Locate every Plasmodium parasite and every leukocyte.
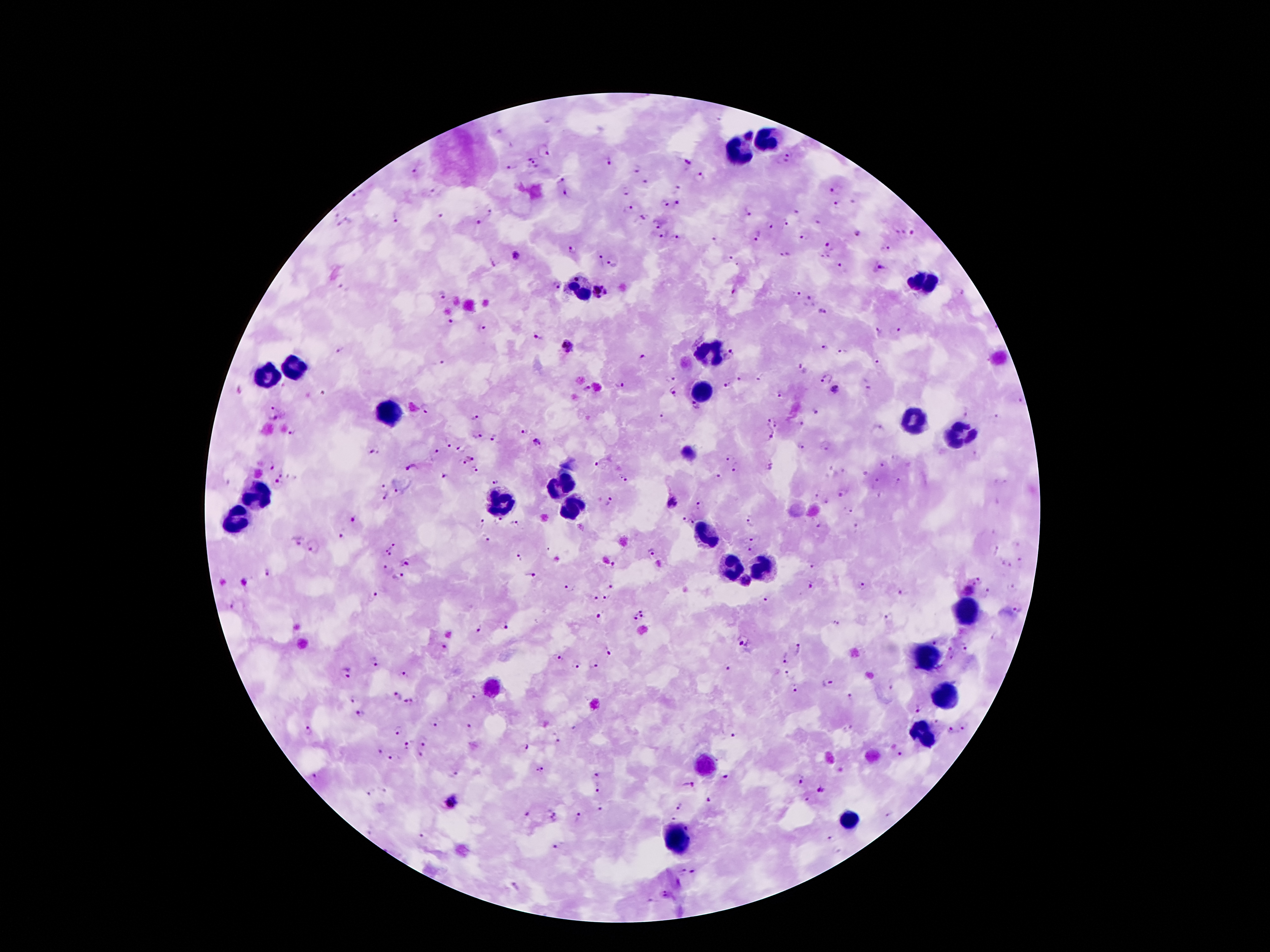

Approximate object centers, in pixels from the top-left corner.
Plasmodium parasites: (x=750, y=137), (x=544, y=150), (x=531, y=156), (x=788, y=158), (x=609, y=160), (x=687, y=161), (x=535, y=164), (x=637, y=168), (x=511, y=169), (x=414, y=171), (x=700, y=176), (x=561, y=178), (x=646, y=181), (x=678, y=187), (x=832, y=189), (x=432, y=191), (x=566, y=191), (x=625, y=191), (x=357, y=193), (x=676, y=202), (x=667, y=203), (x=837, y=206), (x=628, y=208), (x=795, y=210), (x=492, y=212), (x=748, y=212), (x=442, y=216), (x=642, y=216), (x=349, y=219), (x=396, y=219), (x=479, y=222), (x=784, y=223), (x=656, y=224), (x=770, y=225), (x=855, y=232), (x=912, y=233), (x=759, y=234), (x=662, y=235), (x=803, y=236), (x=676, y=238), (x=716, y=240), (x=827, y=245), (x=572, y=250), (x=888, y=250), (x=515, y=255), (x=784, y=255), (x=824, y=258), (x=600, y=259), (x=731, y=259), (x=493, y=262), (x=610, y=264), (x=840, y=266), (x=879, y=269), (x=557, y=285), (x=601, y=291), (x=734, y=291), (x=442, y=294), (x=796, y=295), (x=809, y=301), (x=823, y=311), (x=451, y=322), (x=480, y=328), (x=879, y=331), (x=900, y=331), (x=538, y=337), (x=567, y=346), (x=824, y=349), (x=339, y=350), (x=842, y=351), (x=730, y=355), (x=644, y=356), (x=441, y=363), (x=877, y=364), (x=799, y=366), (x=672, y=378), (x=740, y=378), (x=826, y=379), (x=760, y=380), (x=620, y=386), (x=728, y=386), (x=587, y=388), (x=868, y=389), (x=837, y=391), (x=673, y=393), (x=780, y=395), (x=1020, y=401), (x=274, y=406), (x=696, y=407), (x=425, y=408), (x=818, y=412), (x=966, y=415), (x=997, y=416), (x=475, y=417), (x=663, y=417), (x=272, y=418), (x=768, y=422), (x=802, y=423), (x=775, y=424), (x=879, y=427), (x=524, y=432), (x=292, y=433), (x=477, y=436), (x=770, y=436), (x=493, y=438), (x=535, y=440), (x=448, y=445), (x=801, y=446), (x=826, y=446), (x=459, y=449), (x=436, y=452), (x=374, y=453), (x=472, y=457), (x=727, y=459), (x=461, y=462), (x=598, y=462), (x=271, y=464), (x=883, y=464), (x=769, y=466), (x=410, y=467), (x=735, y=468), (x=475, y=472), (x=864, y=472), (x=281, y=474), (x=444, y=477), (x=624, y=477), (x=718, y=477), (x=877, y=480), (x=898, y=481), (x=494, y=482), (x=277, y=483), (x=382, y=485), (x=395, y=490), (x=818, y=494), (x=841, y=495), (x=383, y=498), (x=609, y=501), (x=673, y=502), (x=827, y=503), (x=699, y=504), (x=849, y=509), (x=684, y=517), (x=352, y=520), (x=692, y=520), (x=751, y=520), (x=499, y=521), (x=482, y=523), (x=513, y=523), (x=818, y=526), (x=856, y=527), (x=341, y=536), (x=753, y=537), (x=487, y=539), (x=296, y=541), (x=393, y=546), (x=750, y=548), (x=313, y=549), (x=995, y=549), (x=652, y=550), (x=387, y=552), (x=518, y=557), (x=1020, y=561), (x=407, y=562), (x=614, y=564), (x=812, y=565), (x=385, y=567), (x=266, y=572), (x=531, y=575), (x=398, y=577), (x=980, y=579), (x=746, y=580), (x=611, y=584), (x=810, y=585), (x=862, y=585), (x=570, y=586), (x=1012, y=587), (x=969, y=590), (x=901, y=592), (x=986, y=592), (x=374, y=595), (x=595, y=596), (x=606, y=598), (x=765, y=599), (x=232, y=606), (x=1017, y=609), (x=639, y=615), (x=598, y=616), (x=888, y=618), (x=836, y=623), (x=504, y=627), (x=479, y=630), (x=744, y=643), (x=934, y=643), (x=795, y=649), (x=950, y=649), (x=965, y=649), (x=607, y=650), (x=785, y=655), (x=558, y=657), (x=953, y=659), (x=374, y=662), (x=595, y=663), (x=577, y=665), (x=726, y=669), (x=345, y=673), (x=404, y=674), (x=790, y=674), (x=829, y=683), (x=796, y=689), (x=397, y=695), (x=851, y=697), (x=473, y=698), (x=351, y=699), (x=411, y=700), (x=917, y=708), (x=360, y=714), (x=937, y=722), (x=435, y=724), (x=963, y=726), (x=469, y=727), (x=307, y=731), (x=397, y=731), (x=951, y=732), (x=733, y=735), (x=424, y=741), (x=558, y=743), (x=406, y=746), (x=523, y=750), (x=380, y=751), (x=420, y=754), (x=900, y=754), (x=395, y=759), (x=539, y=770), (x=455, y=773), (x=596, y=773), (x=312, y=777), (x=726, y=777), (x=800, y=780), (x=690, y=785), (x=821, y=789), (x=596, y=790), (x=385, y=791), (x=369, y=793), (x=710, y=799), (x=807, y=799), (x=451, y=801), (x=677, y=807), (x=601, y=810), (x=527, y=815), (x=554, y=817), (x=577, y=817), (x=672, y=817), (x=420, y=836), (x=829, y=839), (x=557, y=843), (x=682, y=871), (x=692, y=871), (x=666, y=893).
Leukocytes: (x=766, y=143), (x=736, y=153), (x=921, y=284), (x=582, y=290), (x=709, y=354), (x=292, y=365), (x=265, y=378), (x=702, y=395), (x=389, y=415), (x=916, y=422), (x=956, y=434), (x=560, y=483), (x=255, y=496), (x=500, y=505), (x=570, y=506), (x=238, y=516), (x=705, y=538), (x=726, y=567), (x=768, y=569), (x=964, y=612), (x=927, y=658), (x=488, y=687), (x=944, y=701), (x=924, y=733), (x=705, y=764), (x=846, y=822), (x=678, y=838).

Summary:
  - Stain: Giemsa
  - Magnification: 100x
  - Field of view: single
  - Capture: smartphone through the microscope eyepiece
  - Preparation: thick blood film
  - Image size: 1270×952 pixels
  - Patient malaria status: infected with Plasmodium falciparum